Locate every leukocyte (white blood cell).
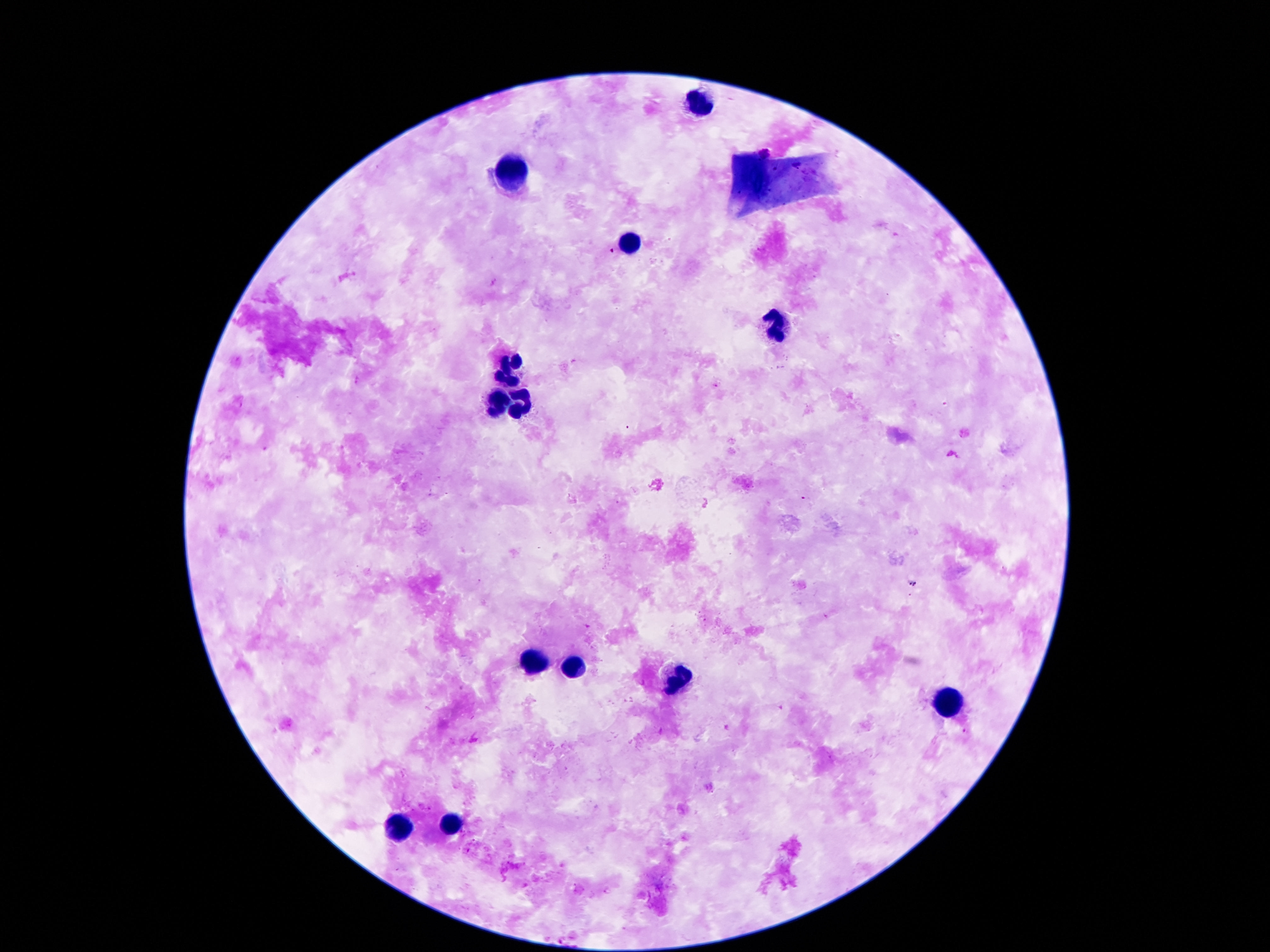

Approximate centers as (x, y) in pixels.
Leukocytes: (700, 104), (514, 172), (628, 239), (778, 326), (509, 366), (498, 399), (521, 405), (531, 663), (570, 668), (679, 679), (947, 702), (450, 821), (399, 827).

Summary:
  - Preparation: thick peripheral-blood smear
  - Magnification: 100x
  - Patient malaria status: uninfected
  - Capture: smartphone camera through the microscope eyepiece
  - Image size: 1270×952 pixels
  - Stain: Giemsa
  - Field of view: one from this slide